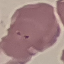 Result: malaria parasites identified. Giemsa stain. Acquired by smartphone through the microscope eyepiece. Cell patch, automatically extracted from a larger field of view and resized to 64 × 64 pixels. Thin blood smear.